Name the parasite shown.
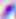
This is Toxoplasma gondii.

Micrograph. 400x magnification.